Assess the morphology of the red blood cells.
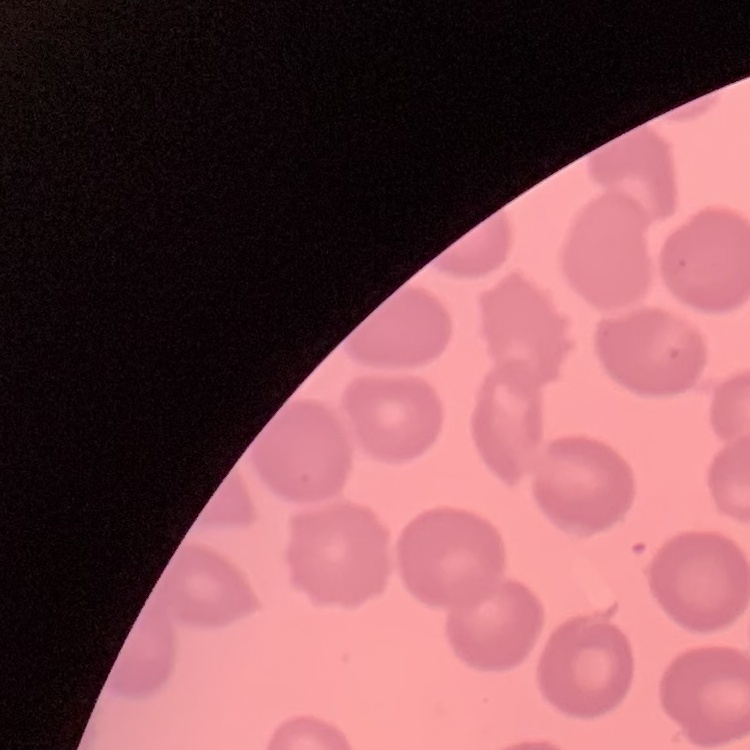

No rouleaux formation.

preparation = thin blood smear
image type = one tile cut from a larger photomicrograph
stain = Field's or Giemsa